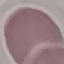

result = no malaria parasites seen
preparation = thin blood smear
capture = smartphone through the microscope eyepiece
stain = Giemsa
image type = automatically extracted cell patch, resized to 64 × 64 pixels